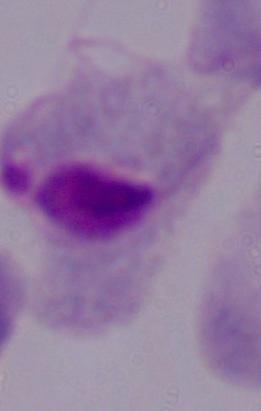

Summary:
  - Identification: trichomonad
  - Modality: photomicrograph
  - Magnification: 1000x